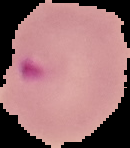

Summary:
  - Image type: segmented cell region on a black background
  - Result: malaria parasites identified
  - Image size: 130×148 pixels
  - Preparation: thin blood smear